State which parasite is depicted.
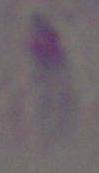

This is Toxoplasma gondii.

Captured at 1000x magnification. Micrograph.